Name the blood parasite species.
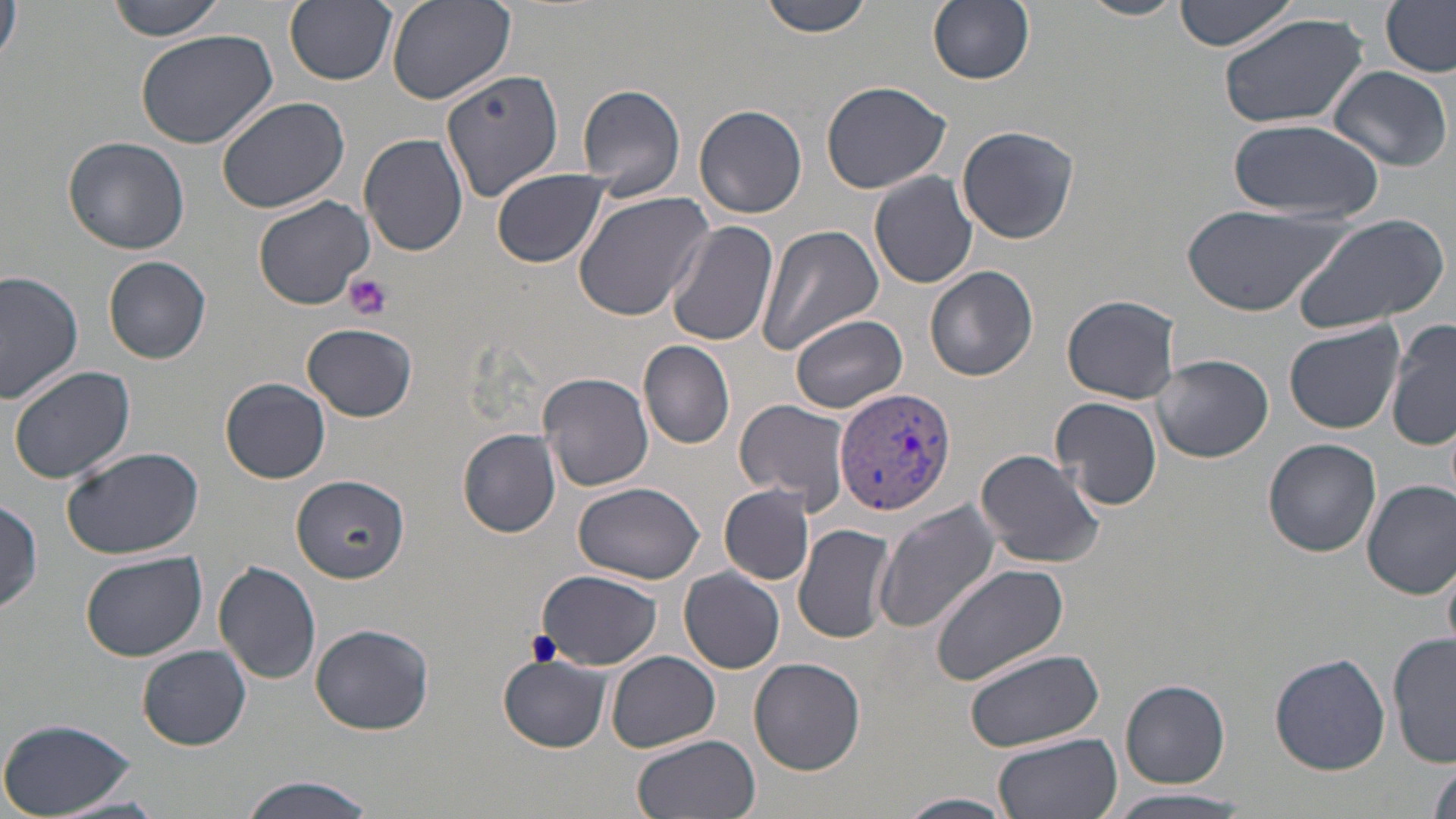
Plasmodium vivax.

Approximate bounding boxes as named x1/y1/x2/y2 corners in pixels. Platelet locations: (x1=345, y1=274, x2=392, y2=320). Plasmodium vivax-infected red blood cell locations: (x1=834, y1=386, x2=956, y2=516). Uninfected red blood cell locations: (x1=1, y1=0, x2=24, y2=71), (x1=105, y1=0, x2=228, y2=40), (x1=286, y1=0, x2=397, y2=86), (x1=384, y1=0, x2=516, y2=104), (x1=760, y1=0, x2=875, y2=38), (x1=928, y1=0, x2=1036, y2=86), (x1=1079, y1=0, x2=1185, y2=23), (x1=1175, y1=0, x2=1297, y2=53), (x1=1379, y1=0, x2=1455, y2=77), (x1=1215, y1=11, x2=1368, y2=131), (x1=135, y1=26, x2=281, y2=150), (x1=1327, y1=65, x2=1453, y2=173), (x1=438, y1=69, x2=565, y2=201), (x1=819, y1=80, x2=950, y2=194), (x1=576, y1=83, x2=687, y2=199), (x1=215, y1=96, x2=350, y2=213), (x1=695, y1=103, x2=808, y2=219), (x1=1228, y1=116, x2=1384, y2=221), (x1=956, y1=125, x2=1079, y2=245), (x1=360, y1=134, x2=468, y2=257), (x1=64, y1=137, x2=189, y2=255), (x1=491, y1=168, x2=609, y2=269), (x1=869, y1=172, x2=979, y2=288), (x1=573, y1=189, x2=716, y2=321), (x1=254, y1=195, x2=374, y2=309), (x1=1180, y1=203, x2=1357, y2=318), (x1=1289, y1=213, x2=1452, y2=333), (x1=666, y1=222, x2=777, y2=349), (x1=758, y1=225, x2=882, y2=356), (x1=102, y1=256, x2=211, y2=362), (x1=926, y1=265, x2=1040, y2=383), (x1=0, y1=272, x2=83, y2=403), (x1=1062, y1=293, x2=1182, y2=404), (x1=791, y1=314, x2=908, y2=413), (x1=1387, y1=315, x2=1456, y2=454), (x1=1285, y1=322, x2=1405, y2=433), (x1=302, y1=323, x2=418, y2=421), (x1=639, y1=340, x2=735, y2=450), (x1=1153, y1=354, x2=1274, y2=463), (x1=7, y1=363, x2=136, y2=485), (x1=537, y1=372, x2=654, y2=495), (x1=221, y1=377, x2=331, y2=483), (x1=1051, y1=395, x2=1163, y2=512), (x1=734, y1=399, x2=851, y2=511), (x1=458, y1=428, x2=563, y2=537), (x1=1262, y1=437, x2=1382, y2=557), (x1=61, y1=446, x2=205, y2=561), (x1=975, y1=448, x2=1104, y2=569), (x1=289, y1=476, x2=409, y2=587), (x1=1362, y1=479, x2=1456, y2=598), (x1=574, y1=481, x2=705, y2=584), (x1=720, y1=485, x2=814, y2=586), (x1=0, y1=499, x2=45, y2=614), (x1=873, y1=502, x2=1001, y2=632), (x1=795, y1=523, x2=897, y2=644), (x1=80, y1=550, x2=207, y2=661), (x1=212, y1=561, x2=322, y2=685), (x1=929, y1=563, x2=1069, y2=684), (x1=678, y1=567, x2=786, y2=674), (x1=536, y1=570, x2=660, y2=669), (x1=309, y1=622, x2=435, y2=734), (x1=1389, y1=633, x2=1456, y2=767), (x1=137, y1=645, x2=252, y2=750), (x1=963, y1=648, x2=1105, y2=752), (x1=605, y1=652, x2=720, y2=752), (x1=1268, y1=652, x2=1393, y2=774), (x1=497, y1=655, x2=612, y2=752), (x1=748, y1=655, x2=866, y2=775), (x1=1120, y1=680, x2=1230, y2=787), (x1=0, y1=717, x2=140, y2=818), (x1=993, y1=733, x2=1122, y2=819), (x1=631, y1=734, x2=761, y2=819), (x1=1425, y1=760, x2=1456, y2=819), (x1=238, y1=774, x2=376, y2=819), (x1=1101, y1=789, x2=1258, y2=819), (x1=897, y1=792, x2=1017, y2=819). Thin blood film. Optical microscopy. 1000x magnification. May-Grünwald-Giemsa stain. One field of a larger specimen. Image is 1456×819 pixels.